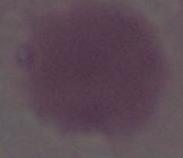

Summary:
  - Identification: red blood cell
  - Modality: photomicrograph
  - Magnification: 1000x